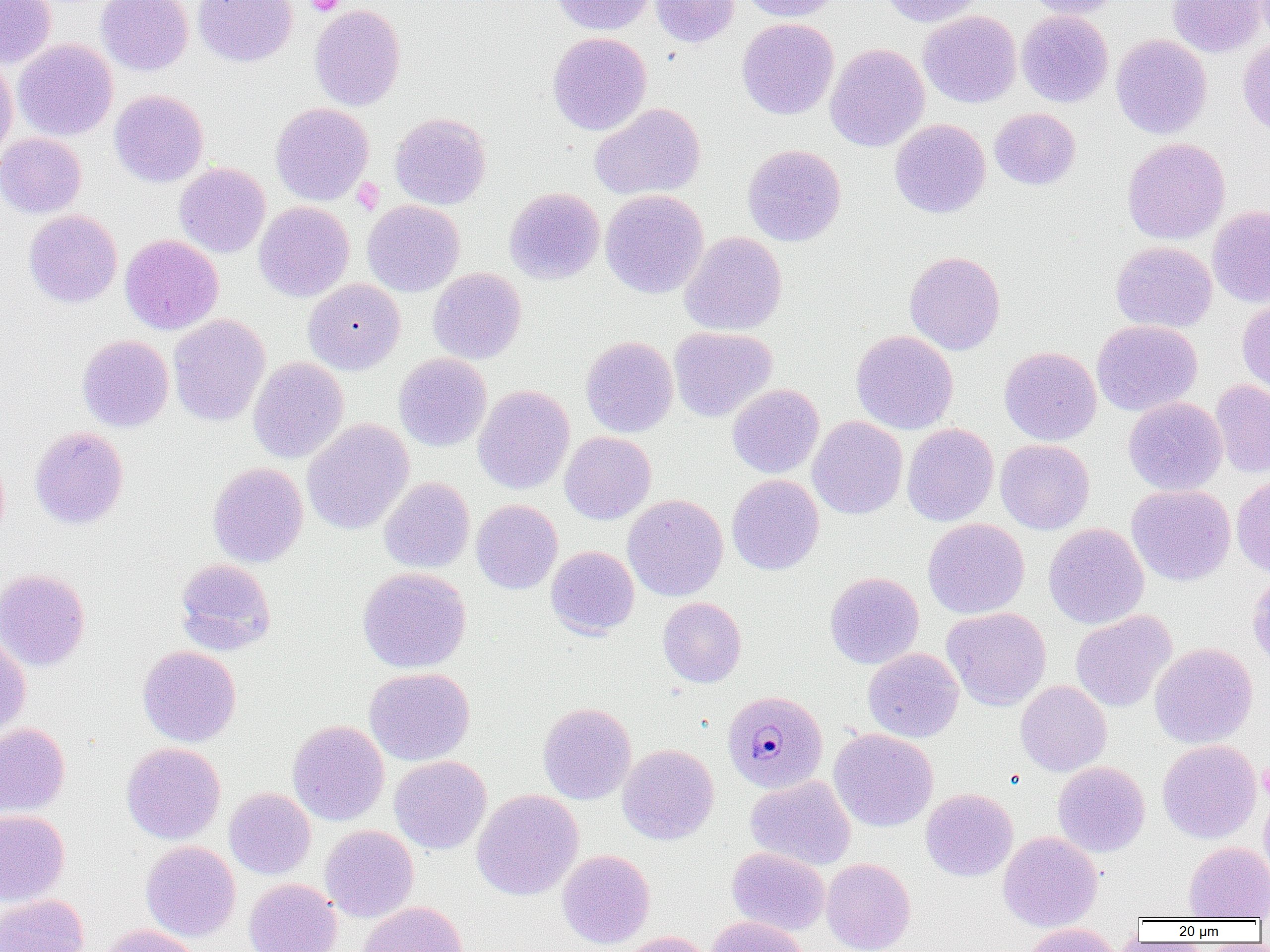

slide-level diagnosis = Plasmodium malariae
preparation = thin blood smear
image size = 1270×952 pixels
magnification = 1000x
field of view = single
platelet locations = approximate bounding boxes as (x1,y1)-(x2,y2) corner pairs in pixels: (305,0)-(344,16), (351,178)-(384,215), (1259,761)-(1270,800)
modality = optical microscopy
Plasmodium malariae-infected red blood cell locations = approximate bounding boxes as (x1,y1)-(x2,y2) corner pairs in pixels: (724,692)-(829,795)
uninfected red blood cell locations = approximate bounding boxes as (x1,y1)-(x2,y2) corner pairs in pixels: (0,0)-(56,68), (96,0)-(194,75), (193,0)-(297,67), (549,0)-(655,36), (649,0)-(739,47), (738,0)-(842,22), (881,0)-(985,27), (1021,0)-(1127,19), (1167,0)-(1268,57), (309,3)-(406,111), (918,10)-(1021,108), (1016,10)-(1113,108), (736,18)-(839,120), (547,32)-(652,135), (1111,34)-(1212,138), (1237,37)-(1270,138), (13,39)-(118,140), (825,43)-(930,152), (0,60)-(17,163), (109,90)-(208,187), (270,102)-(374,206), (590,103)-(706,201), (989,108)-(1081,190), (390,112)-(492,210), (890,118)-(991,218), (0,132)-(86,218), (1121,137)-(1230,245), (742,144)-(846,247), (174,163)-(270,258), (504,187)-(604,285), (600,189)-(708,299), (362,200)-(464,296), (254,201)-(354,301), (1207,206)-(1270,308), (24,210)-(122,308), (679,231)-(787,336), (120,234)-(223,334), (1110,241)-(1217,333), (904,251)-(1006,355), (428,268)-(526,364), (303,279)-(405,375), (1237,298)-(1270,394), (168,314)-(270,426), (1091,320)-(1202,416), (669,327)-(777,422), (851,329)-(959,434), (77,334)-(174,432), (581,336)-(678,437), (999,346)-(1101,445), (394,353)-(492,452), (248,357)-(349,464), (1210,379)-(1270,478), (473,384)-(575,494), (727,384)-(824,478), (1123,396)-(1228,495), (807,416)-(908,519), (302,419)-(414,535), (902,424)-(999,526), (29,426)-(129,530), (560,431)-(656,524), (995,439)-(1094,534), (207,462)-(309,567), (727,474)-(824,575), (1231,474)-(1270,579), (379,477)-(475,573), (1126,484)-(1236,586), (623,494)-(728,601), (471,499)-(563,594), (923,518)-(1029,619), (1043,523)-(1149,629), (546,546)-(639,638), (175,558)-(276,655), (357,567)-(472,673), (0,568)-(91,672), (824,571)-(924,669), (1246,571)-(1270,669), (657,597)-(746,688), (942,607)-(1051,711), (1071,610)-(1176,712), (0,635)-(31,739), (1149,642)-(1257,748), (137,645)-(241,747), (863,647)-(964,743), (364,667)-(475,766), (1015,681)-(1112,776), (537,702)-(636,804), (288,720)-(389,826), (0,722)-(70,818), (829,729)-(938,832), (1157,739)-(1262,844), (122,742)-(225,844), (617,744)-(719,845), (390,755)-(492,854), (1053,761)-(1150,857), (746,775)-(855,870), (1259,787)-(1270,887), (224,788)-(316,879), (921,788)-(1018,881), (472,789)-(584,900), (0,809)-(70,906), (320,825)-(419,923), (998,831)-(1104,931), (140,841)-(241,942), (1183,841)-(1270,920), (727,847)-(830,935), (557,849)-(655,949), (821,858)-(916,952), (243,878)-(342,952), (0,894)-(89,952), (355,901)-(469,952), (706,915)-(809,952), (1023,923)-(1123,952), (94,925)-(203,952), (617,932)-(714,952)